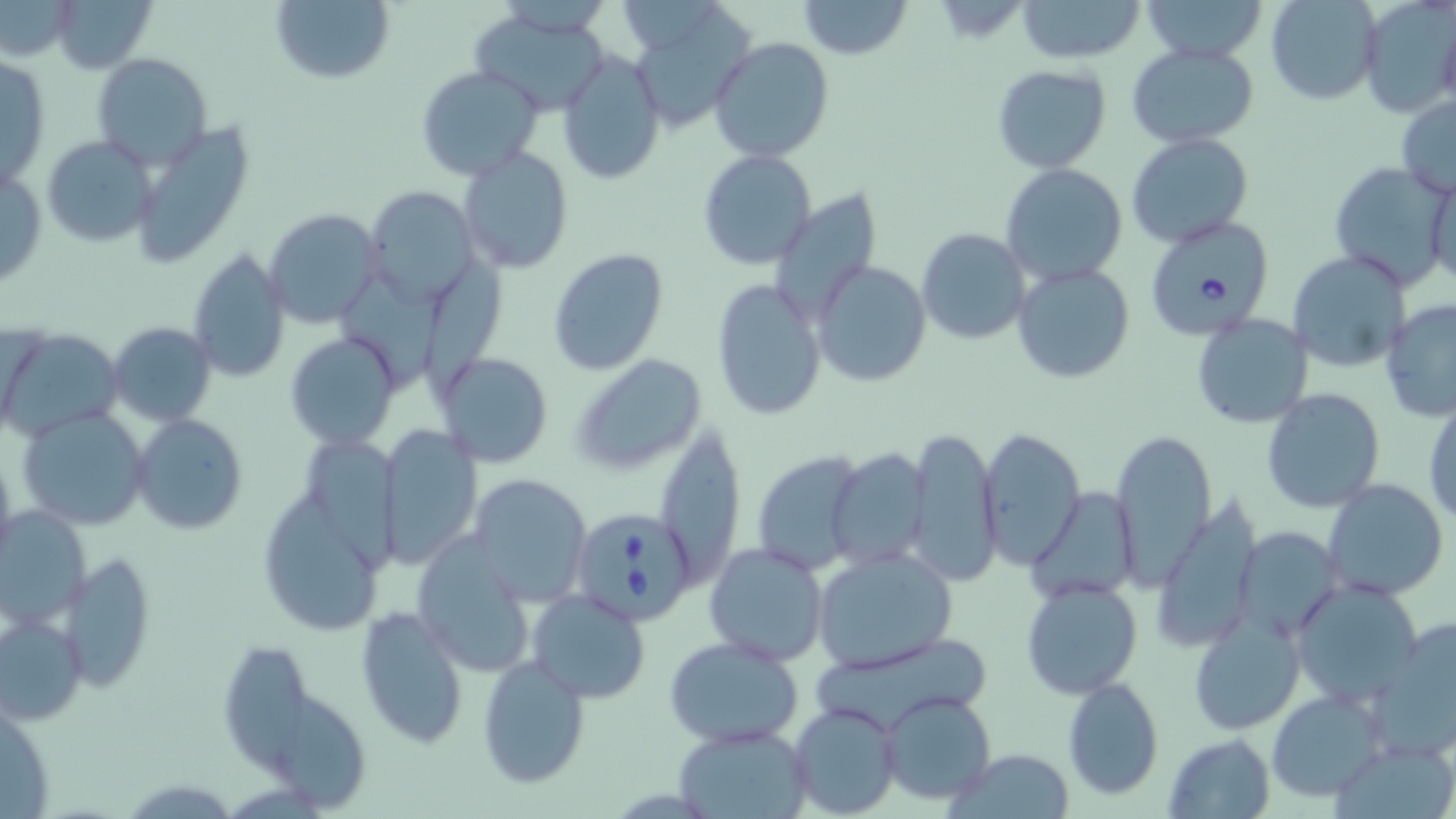

Approximate bounding boxes as [x1, y1, x2, y2] in pixels. Babesia divergens-infected red blood cell locations: [1141, 214, 1275, 335], [569, 506, 699, 625]. Uninfected red blood cell locations: [47, 0, 156, 73], [269, 0, 394, 86], [795, 0, 914, 59], [1017, 0, 1145, 63], [1143, 0, 1271, 60], [1266, 1, 1381, 104], [1358, 1, 1454, 119], [466, 7, 615, 117], [629, 10, 762, 127], [1438, 16, 1456, 113], [709, 36, 834, 162], [1126, 42, 1260, 147], [558, 49, 664, 187], [93, 54, 212, 168], [1, 56, 51, 193], [415, 65, 544, 181], [992, 65, 1111, 174], [1396, 96, 1456, 199], [1126, 132, 1254, 249], [41, 135, 156, 249], [459, 147, 574, 273], [698, 150, 818, 272], [1328, 161, 1453, 289], [1000, 162, 1129, 287], [1, 163, 47, 292], [1425, 173, 1456, 291], [362, 186, 482, 307], [776, 188, 882, 320], [263, 210, 381, 327], [916, 228, 1032, 345], [186, 249, 291, 381], [548, 249, 669, 375], [1287, 250, 1411, 373], [430, 252, 511, 397], [810, 260, 932, 387], [1011, 262, 1134, 384], [341, 274, 449, 394], [712, 279, 828, 421], [1381, 301, 1456, 422], [1190, 313, 1314, 428], [106, 323, 216, 425], [0, 328, 121, 440], [286, 334, 401, 450], [436, 352, 553, 467], [571, 354, 708, 474], [1261, 387, 1386, 513], [1424, 392, 1456, 527], [17, 407, 153, 530], [132, 415, 248, 533], [654, 423, 744, 588], [375, 426, 481, 569], [907, 427, 1002, 587], [1108, 427, 1216, 586], [977, 429, 1084, 570], [309, 438, 412, 576], [0, 445, 18, 576], [826, 447, 932, 571], [751, 450, 870, 573], [470, 472, 592, 605], [259, 476, 390, 643], [1322, 478, 1449, 601], [1029, 487, 1142, 600], [0, 509, 91, 629], [1237, 526, 1342, 641], [409, 535, 538, 677], [702, 542, 829, 667], [811, 548, 955, 673], [59, 550, 156, 691], [1021, 579, 1142, 698], [1290, 579, 1424, 707], [527, 589, 651, 702], [356, 607, 469, 746], [0, 613, 87, 725], [1188, 614, 1304, 735], [1369, 615, 1456, 764], [663, 635, 807, 748], [811, 635, 991, 736], [225, 642, 309, 774], [477, 654, 590, 789], [1062, 677, 1164, 801], [1266, 689, 1386, 800], [281, 690, 370, 812], [880, 691, 997, 805], [789, 701, 902, 818], [672, 723, 810, 817], [1163, 734, 1275, 817], [949, 748, 1076, 819]. Slide-level diagnosis: Babesia divergens. Thin blood film. Single field of view. May-Grünwald-Giemsa-stained preparation. Captured at 1000x magnification. Light microscopy. Image is 1456×819 pixels.